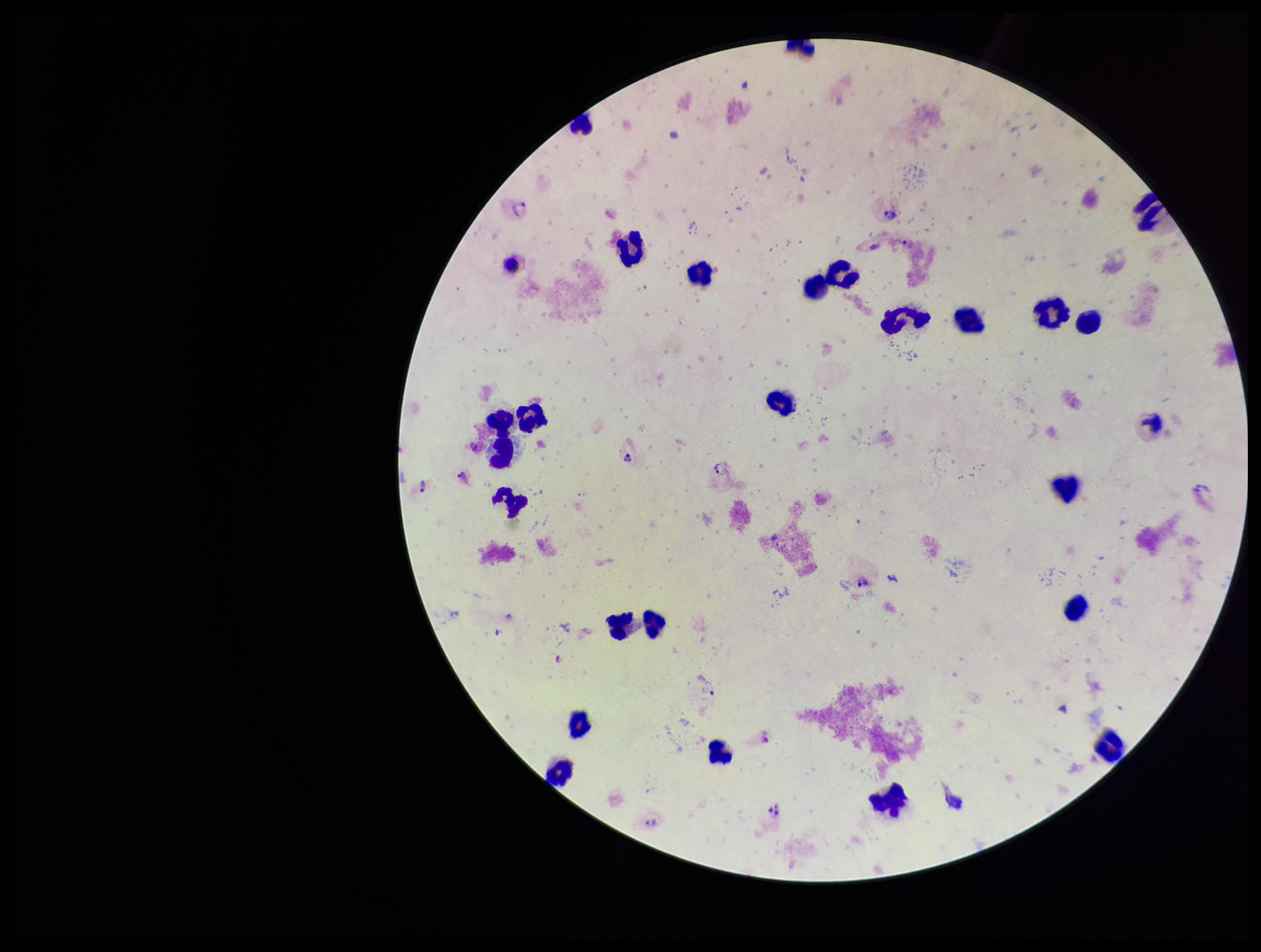
patient malaria status = positive
leukocyte count = 25
species reported for this patient = Plasmodium vivax
stain = Giemsa
image size = 1261×952 pixels
field of view = single
capture = smartphone photograph through the microscope eyepiece
parasite count = 9
Plasmodium parasites = detected
preparation = thick